Assess this cell for malaria.
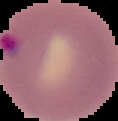

Parasitized.

Summary:
  - Preparation: thin blood film
  - Image size: 118×121 pixels
  - Image type: segmented cell region with the area outside set to black